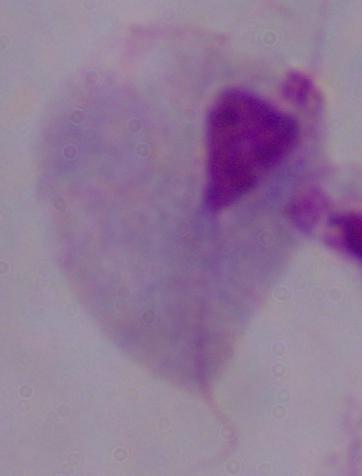

modality = micrograph
identification = trichomonad
magnification = 1000x